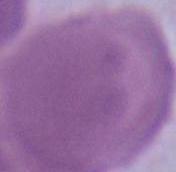
identification: erythrocyte
modality: photomicrograph
magnification: 1000x